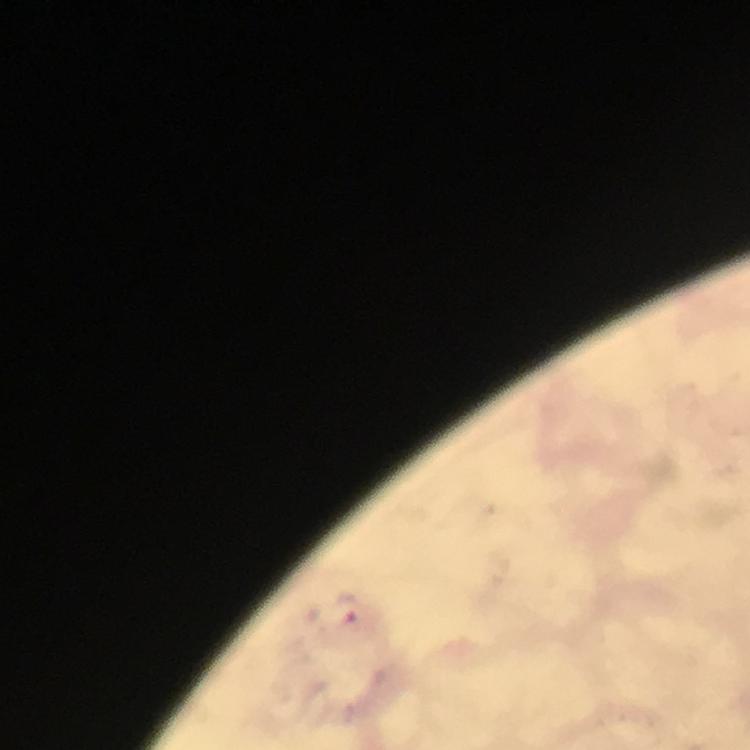
image size = 750×750 pixels
capture = smartphone camera through the microscope
immersion oil = applied
magnification = 100x
Plasmodium parasite locations = approximate centers as {x, y} in pixels: {343, 607}
context = from a diagnostic examination for malaria
stain = Giemsa
cropped from = a single field of view
preparation = thick blood film